Identify the preparation type.
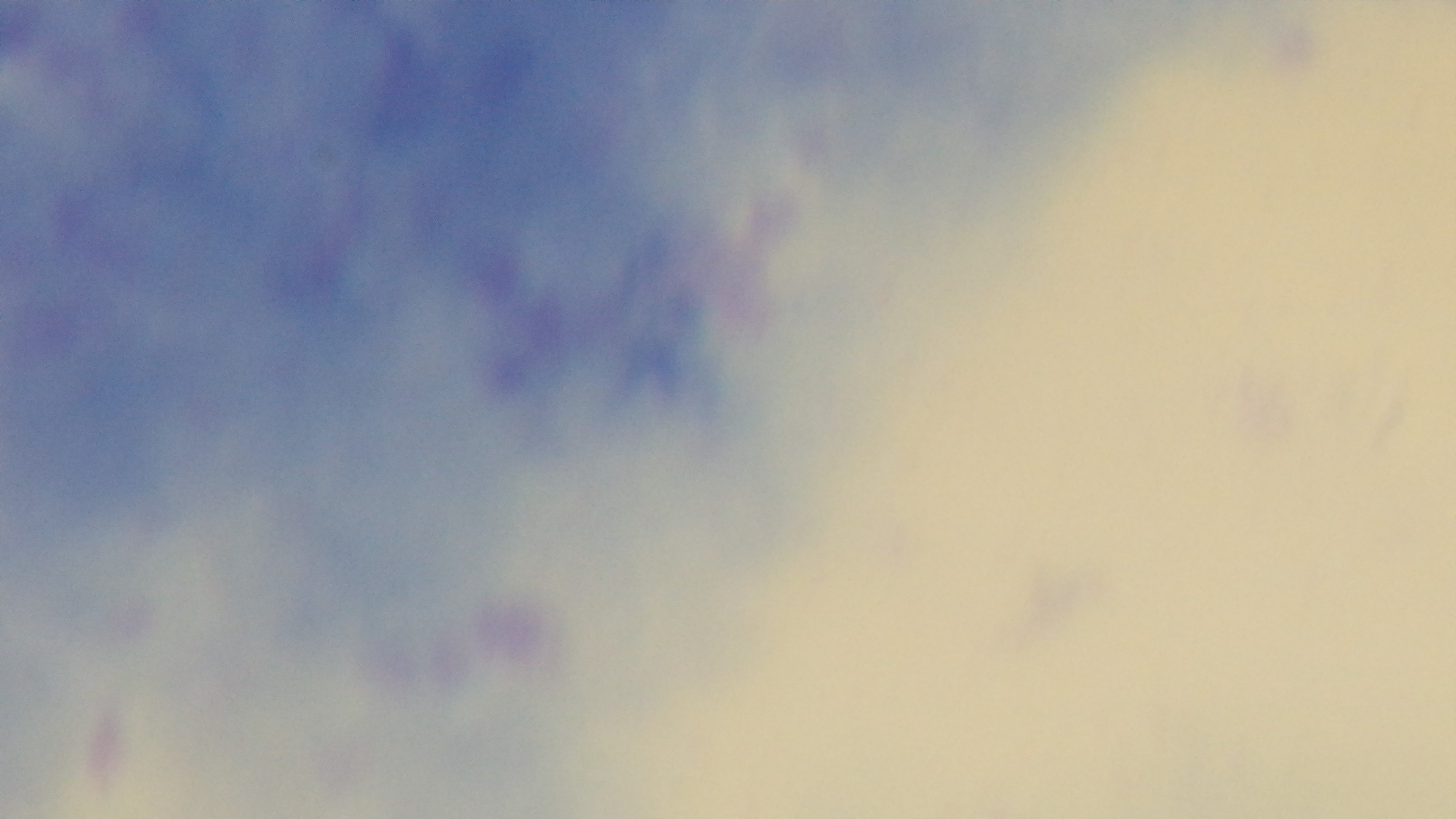

It is a thick blood film.

Summary:
  - Objective: 100x oil immersion
  - Stain: Giemsa
  - Field of view: one from the slide
  - Capture: mounted 4K digital camera
  - Modality: light microscopy
  - Malaria status: negative